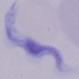
Summary:
  - Magnification: 1000x
  - Modality: micrograph
  - Identification: trypanosome